Name the parasite shown.
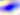
Toxoplasma gondii.

Captured at 400x magnification. Micrograph.